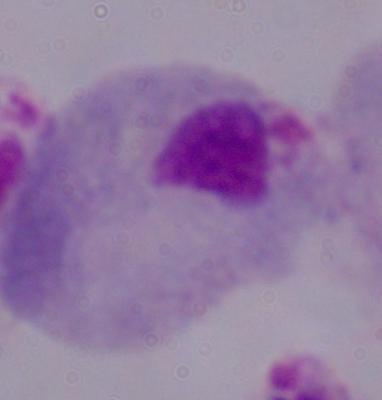
Photomicrograph. Captured at 1000x magnification. A trichomonad is shown.